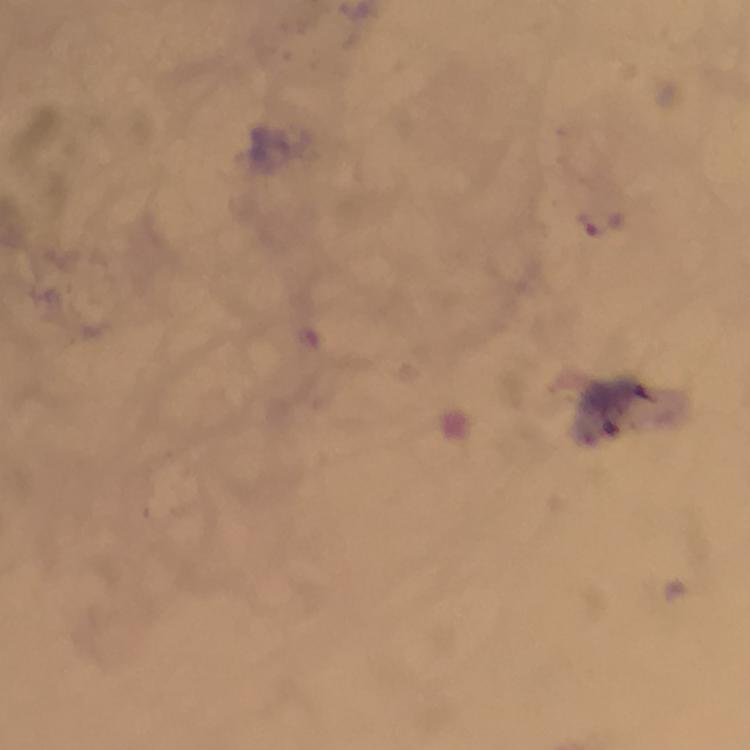
{
  "capture": "smartphone camera through the microscope",
  "magnification": "100x",
  "context": "from a diagnostic examination for malaria",
  "cropped_from": "a single field of view",
  "stain": "Giemsa",
  "immersion_oil": "applied",
  "malaria_parasite_locations": "approximate object centers, in pixels from the top-left corner: (x=604, y=224)",
  "image_size": "750×750 pixels",
  "preparation": "thick blood film"
}